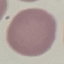
{
  "malaria_status": "uninfected",
  "capture": "smartphone camera at the microscope eyepiece",
  "preparation": "thin blood smear",
  "stain": "Giemsa",
  "image_type": "cell patch, automatically extracted from a larger field of view and resized to 64 × 64 pixels"
}